Outline each blood parasite and name the species.
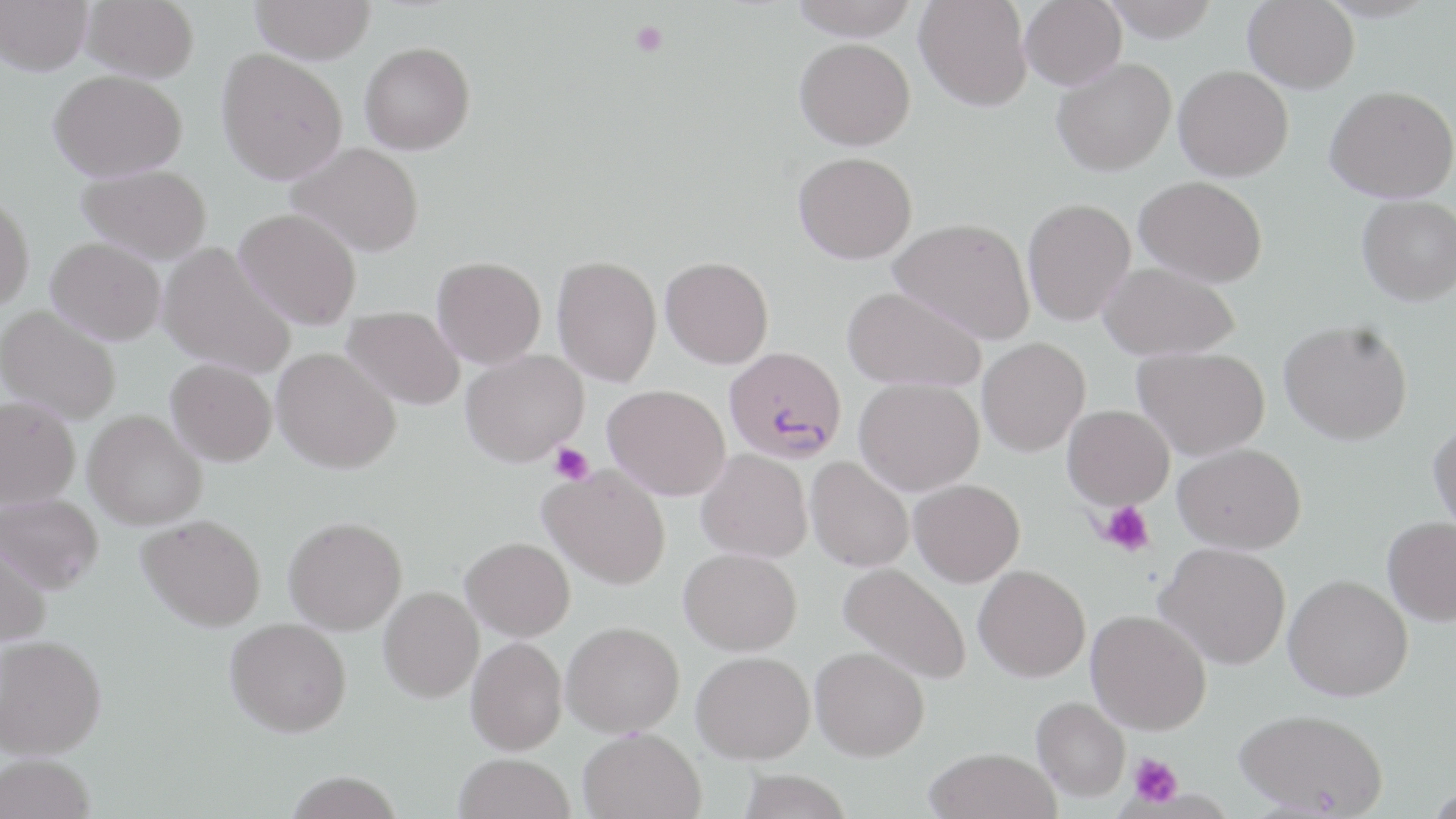
Approximate bounding boxes as (x1,y1)-(x2,y2) corner pairs in pixels.
Plasmodium falciparum-infected red blood cells: (723,346)-(847,464).
No Plasmodium ovale, Plasmodium malariae, Plasmodium vivax, Babesia divergens, or Trypanosoma brucei observed.

Platelet locations: (631,21)-(668,56), (549,442)-(594,485), (1100,500)-(1155,558), (1128,753)-(1182,807). Uninfected red blood cell locations: (0,0)-(94,75), (82,0)-(199,82), (251,0)-(375,64), (789,0)-(919,40), (914,0)-(1031,111), (1020,0)-(1126,90), (1100,0)-(1221,41), (1243,0)-(1359,93), (794,37)-(915,150), (360,41)-(475,154), (216,49)-(348,184), (1052,57)-(1176,175), (1173,65)-(1293,181), (48,69)-(187,182), (1325,85)-(1456,202), (286,142)-(424,257), (793,151)-(917,263), (77,164)-(213,264), (1135,176)-(1268,287), (0,193)-(35,310), (1357,194)-(1456,305), (1022,198)-(1136,325), (234,208)-(362,329), (888,217)-(1035,343), (46,236)-(166,345), (158,242)-(296,379), (552,254)-(662,387), (432,256)-(546,368), (660,256)-(774,368), (1098,262)-(1240,360), (842,286)-(986,392), (0,306)-(121,424), (343,306)-(465,410), (1279,320)-(1413,445), (978,337)-(1090,456), (1133,346)-(1270,460), (273,347)-(401,474), (460,350)-(588,466), (166,358)-(277,466), (854,377)-(984,495), (603,384)-(730,499), (0,396)-(80,509), (1063,405)-(1174,509), (83,410)-(207,530), (1428,421)-(1456,536), (1173,442)-(1306,554), (696,450)-(812,562), (806,456)-(914,572), (540,465)-(671,589), (909,479)-(1025,586), (1,493)-(103,593), (137,514)-(266,631), (283,516)-(407,635), (1382,517)-(1456,625), (0,537)-(51,646), (461,537)-(575,641), (1157,542)-(1291,669), (679,547)-(802,655), (839,562)-(972,684), (974,565)-(1090,681), (1283,574)-(1413,701), (378,586)-(484,702), (1087,609)-(1211,734), (225,617)-(352,736), (561,621)-(685,737), (0,634)-(106,759), (466,637)-(567,754), (810,646)-(930,760), (692,651)-(815,763), (1032,696)-(1130,800), (1235,707)-(1388,817), (577,727)-(706,819), (924,747)-(1061,819), (453,753)-(576,819), (0,754)-(96,818), (737,769)-(853,819), (285,772)-(403,818). Slide-level diagnosis: Plasmodium falciparum. Image is 1456×819 pixels. Single field of view. Thin blood film. Light microscopy. May-Grünwald-Giemsa-stained preparation. 1000x magnification.